State the preparation type.
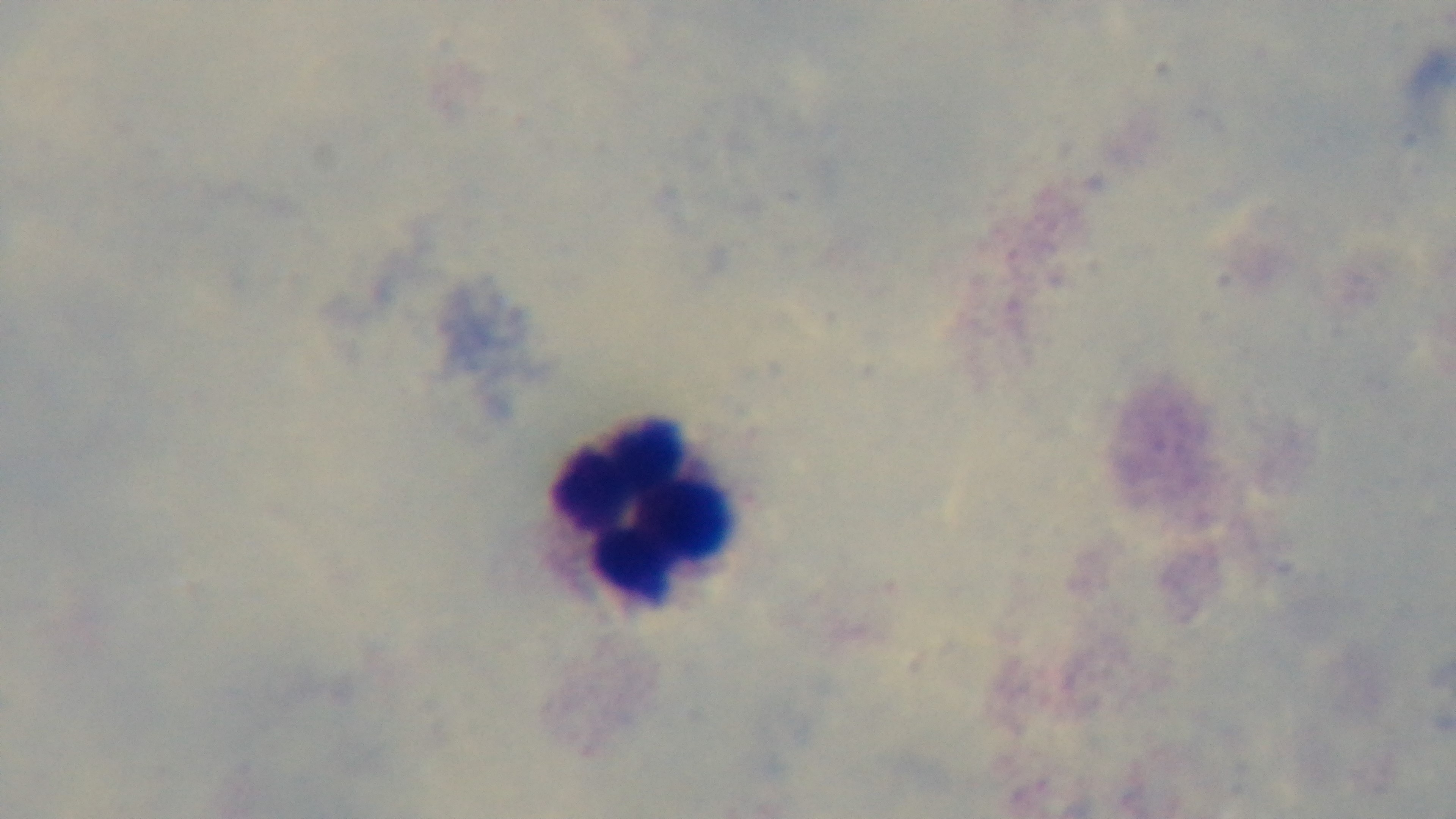

Thick.

Summary:
  - Capture: mounted 4K digital camera
  - Modality: light microscopy
  - Stain: Giemsa
  - Objective: 100x oil immersion
  - Malaria status: negative
  - Field of view: single